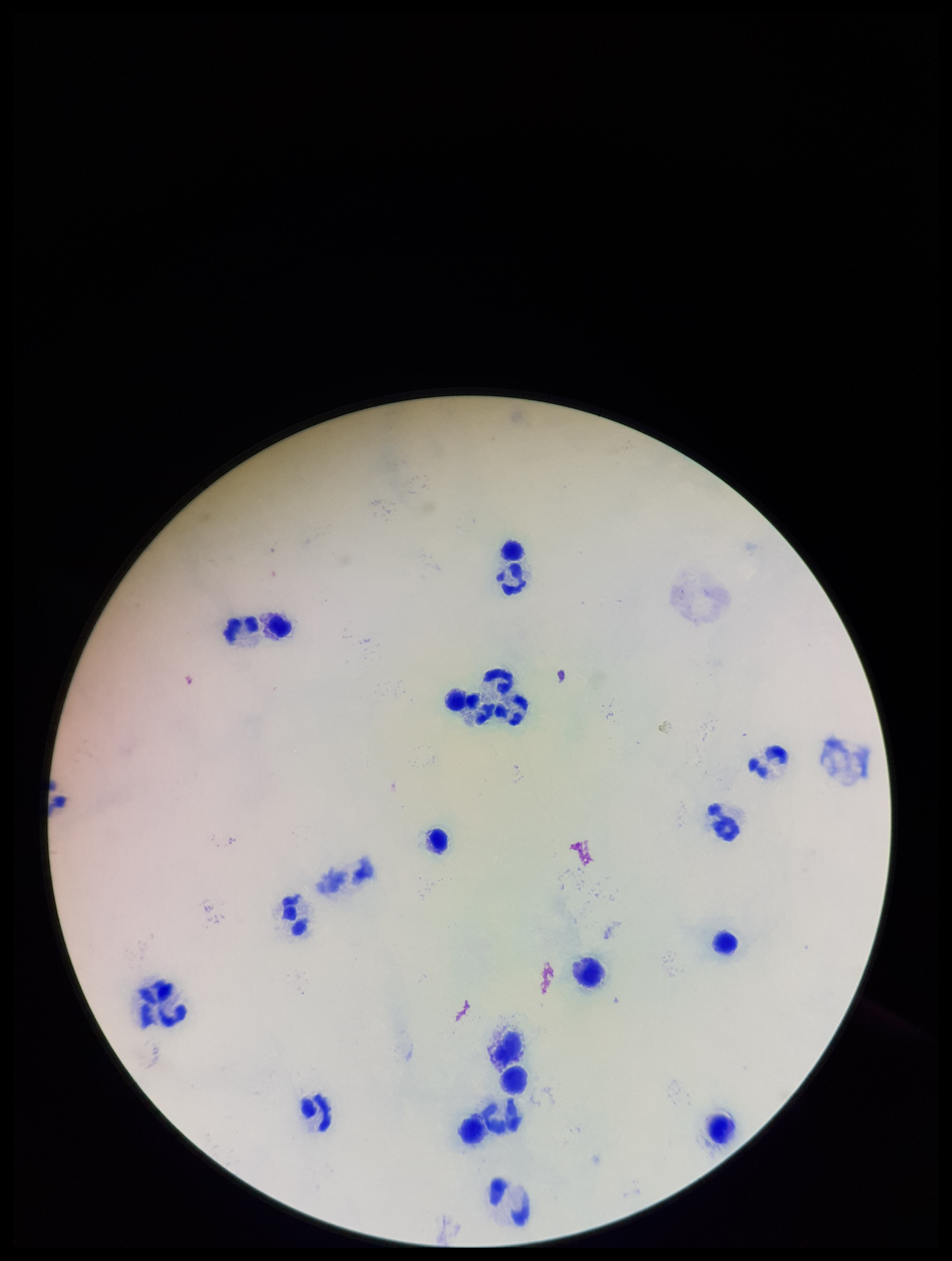
Parasite count: 0. Preparation: thick. Single field of view. Smartphone photograph taken through the eyepiece of a microscope. Plasmodium parasites: none detected. Giemsa stain. Patient malaria status: negative. Image is 952×1261 pixels. Leukocyte count: 22.